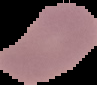
image type = segmented cell region with the area outside set to black
preparation = thin blood film
result = no Plasmodium parasites detected
image size = 97×85 pixels